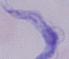 A trypanosome is seen. 1000x magnification. Micrograph.